Describe the morphology of the red blood cells.
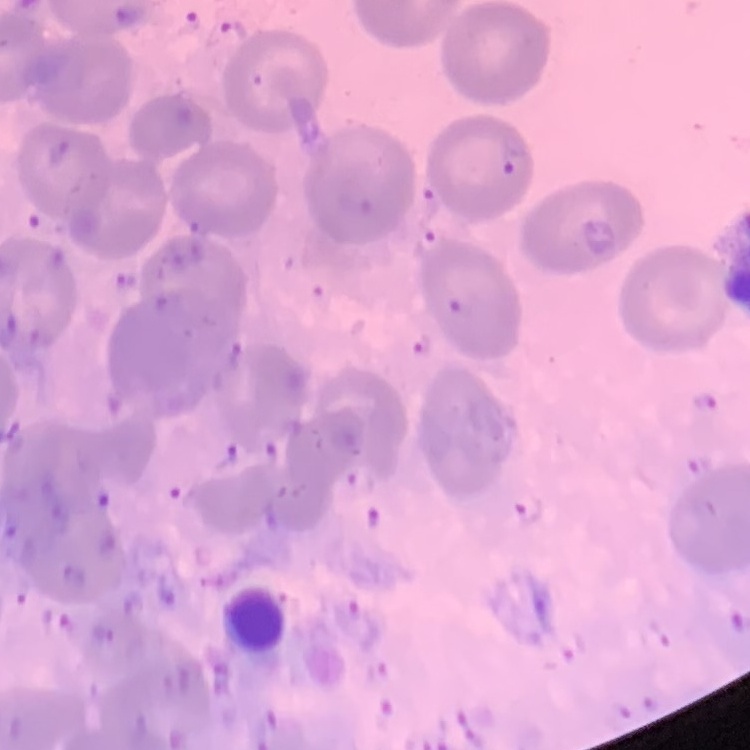

They show no rouleaux formation.

stain = Field's or Giemsa
image type = one tile cut from a larger photomicrograph
preparation = thin blood smear